Assess this cell for malaria.
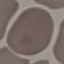

Uninfected.

Thin blood smear. Automatically extracted cell patch, resized to 64 × 64 pixels. Photographed with a smartphone camera at the microscope eyepiece. Giemsa stain.